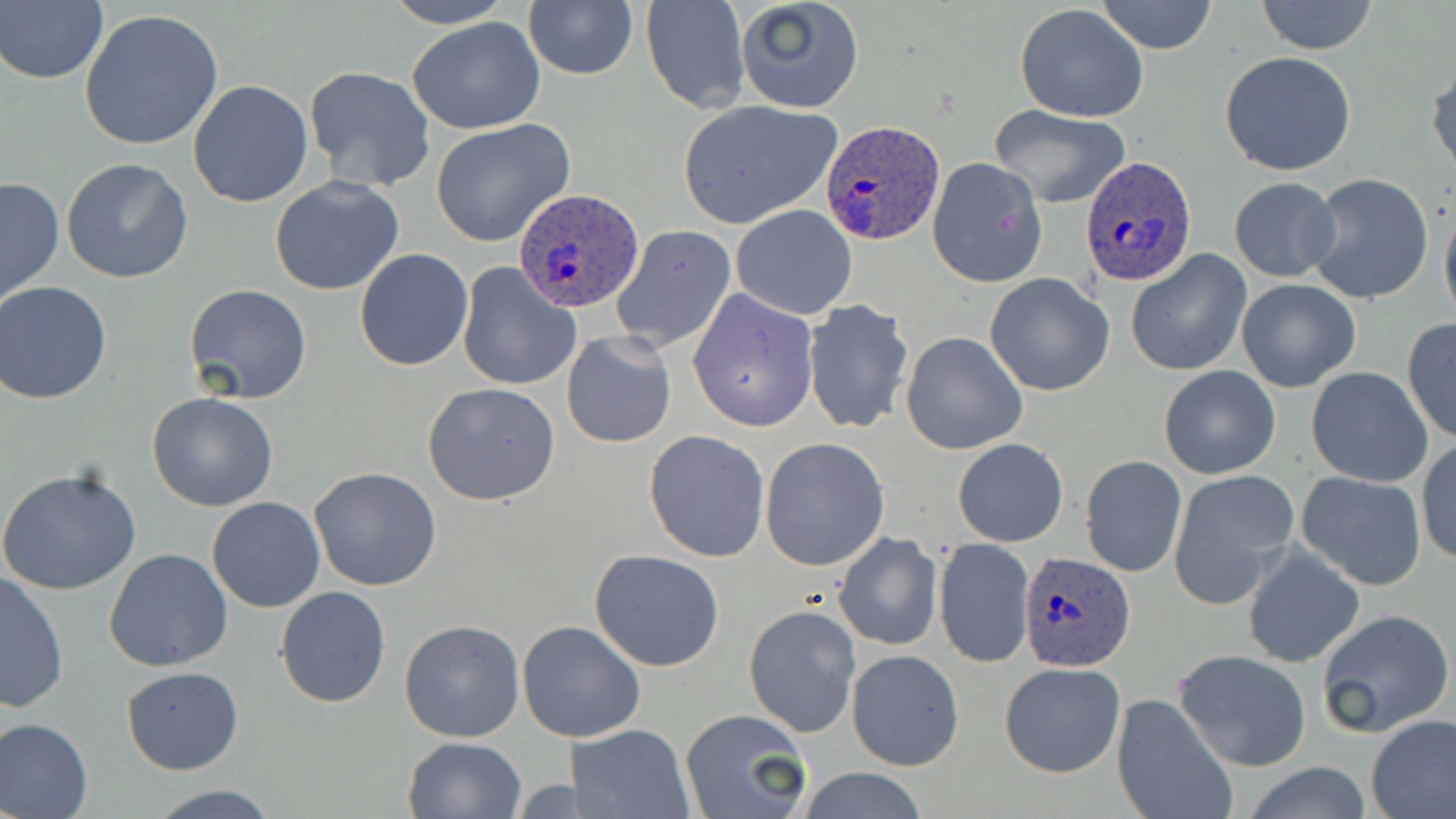
Approximate bounding boxes as named x1/y1/x2/y2 corners in pixels. Plasmodium ovale-infected red blood cell locations: (x1=819, y1=120, x2=946, y2=245), (x1=1081, y1=156, x2=1198, y2=285), (x1=511, y1=188, x2=643, y2=312), (x1=1019, y1=550, x2=1138, y2=671). Uninfected red blood cell locations: (x1=381, y1=0, x2=516, y2=29), (x1=522, y1=0, x2=638, y2=80), (x1=734, y1=0, x2=864, y2=114), (x1=1097, y1=0, x2=1218, y2=54), (x1=1256, y1=0, x2=1378, y2=55), (x1=641, y1=1, x2=750, y2=114), (x1=1, y1=2, x2=109, y2=85), (x1=1015, y1=5, x2=1149, y2=124), (x1=78, y1=8, x2=226, y2=152), (x1=406, y1=17, x2=547, y2=134), (x1=1219, y1=51, x2=1357, y2=175), (x1=1428, y1=60, x2=1456, y2=181), (x1=303, y1=65, x2=436, y2=193), (x1=187, y1=79, x2=313, y2=208), (x1=678, y1=101, x2=840, y2=230), (x1=988, y1=105, x2=1132, y2=209), (x1=430, y1=120, x2=577, y2=249), (x1=62, y1=157, x2=194, y2=285), (x1=927, y1=157, x2=1046, y2=287), (x1=1306, y1=173, x2=1434, y2=304), (x1=0, y1=175, x2=65, y2=310), (x1=269, y1=176, x2=404, y2=296), (x1=1229, y1=177, x2=1340, y2=282), (x1=1439, y1=196, x2=1456, y2=330), (x1=730, y1=204, x2=858, y2=320), (x1=610, y1=223, x2=736, y2=354), (x1=354, y1=248, x2=473, y2=370), (x1=1126, y1=251, x2=1252, y2=376), (x1=455, y1=261, x2=582, y2=392), (x1=985, y1=273, x2=1114, y2=395), (x1=1236, y1=279, x2=1361, y2=392), (x1=1, y1=281, x2=116, y2=404), (x1=184, y1=283, x2=312, y2=404), (x1=687, y1=289, x2=818, y2=433), (x1=803, y1=299, x2=917, y2=436), (x1=1401, y1=319, x2=1456, y2=443), (x1=561, y1=331, x2=677, y2=450), (x1=902, y1=332, x2=1028, y2=455), (x1=1159, y1=365, x2=1280, y2=479), (x1=1305, y1=366, x2=1435, y2=488), (x1=422, y1=382, x2=561, y2=505), (x1=147, y1=391, x2=278, y2=512), (x1=643, y1=429, x2=770, y2=561), (x1=760, y1=438, x2=890, y2=571), (x1=952, y1=438, x2=1068, y2=547), (x1=1416, y1=439, x2=1455, y2=566), (x1=1080, y1=455, x2=1186, y2=577), (x1=309, y1=467, x2=442, y2=591), (x1=0, y1=468, x2=142, y2=597), (x1=1169, y1=470, x2=1298, y2=606), (x1=1295, y1=471, x2=1427, y2=591), (x1=206, y1=496, x2=326, y2=612), (x1=833, y1=532, x2=942, y2=650), (x1=934, y1=537, x2=1034, y2=669), (x1=1241, y1=544, x2=1364, y2=669), (x1=104, y1=548, x2=233, y2=672), (x1=589, y1=549, x2=726, y2=671), (x1=0, y1=571, x2=70, y2=713), (x1=275, y1=586, x2=392, y2=708), (x1=744, y1=604, x2=861, y2=738), (x1=1316, y1=608, x2=1454, y2=738), (x1=398, y1=619, x2=526, y2=742), (x1=518, y1=621, x2=644, y2=742), (x1=847, y1=649, x2=964, y2=771), (x1=1173, y1=649, x2=1312, y2=772), (x1=1000, y1=662, x2=1125, y2=778), (x1=121, y1=666, x2=242, y2=775), (x1=1113, y1=691, x2=1236, y2=819), (x1=681, y1=709, x2=812, y2=819), (x1=1365, y1=715, x2=1456, y2=819), (x1=0, y1=717, x2=94, y2=818), (x1=571, y1=724, x2=693, y2=819), (x1=402, y1=736, x2=527, y2=819), (x1=1241, y1=763, x2=1374, y2=818), (x1=789, y1=768, x2=934, y2=819), (x1=508, y1=778, x2=585, y2=816), (x1=145, y1=784, x2=279, y2=818). Slide-level diagnosis: Plasmodium ovale. May-Grünwald-Giemsa-stained preparation. Captured at 1000x magnification. Optical microscopy. One field of a larger specimen. Image is 1456×819 pixels. Thin blood film.